State the preparation type.
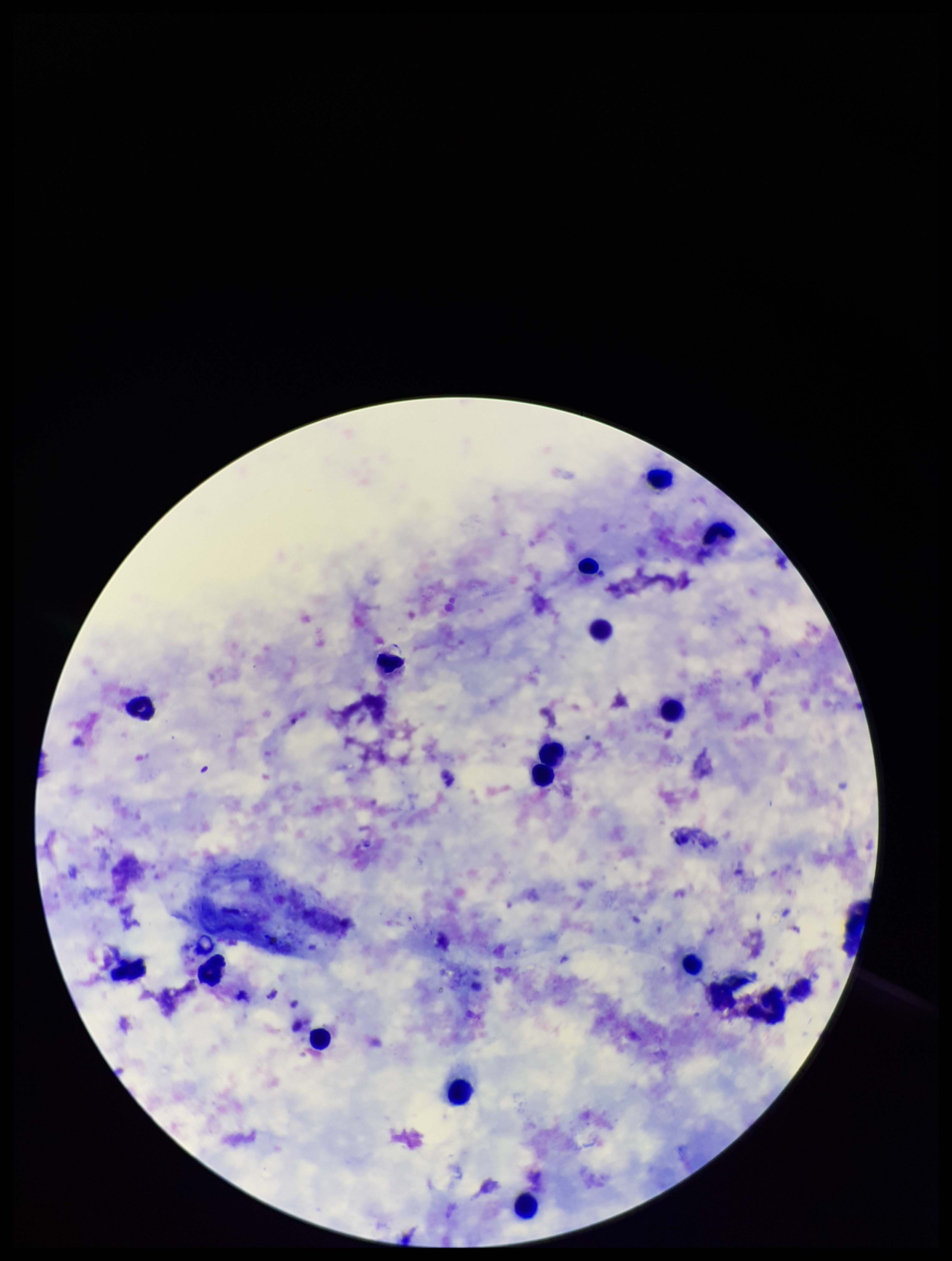

Thick.

Plasmodium parasites: none seen. Leukocyte count: 17. Parasite count: 0. Image is 952×1261 pixels. Stained with Giemsa. Patient malaria status: negative. Smartphone photograph taken through the eyepiece of a microscope. One field from this slide.